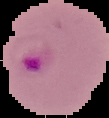
Summary:
  - Image size: 109×118 pixels
  - Preparation: thin blood smear
  - Malaria status: parasitized
  - Image type: cell region segmented out of the field of view; surrounding area masked to black